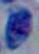

Toxoplasma gondii is seen. Photomicrograph. 1000x magnification.